Comment on the morphology of the erythrocytes.
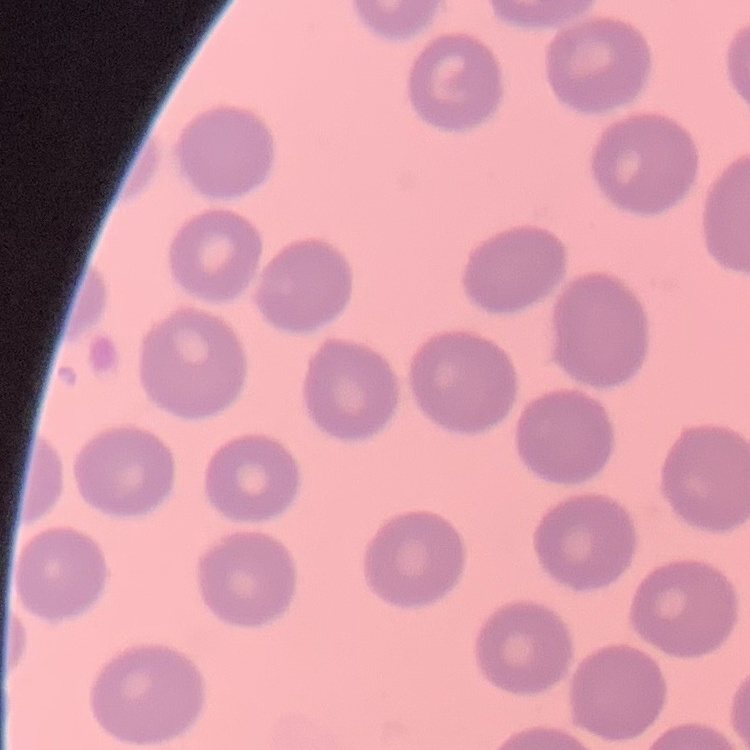

They show no rouleaux formation.

Field's or Giemsa stain. One tile cut from a larger photomicrograph. Thin peripheral smear.